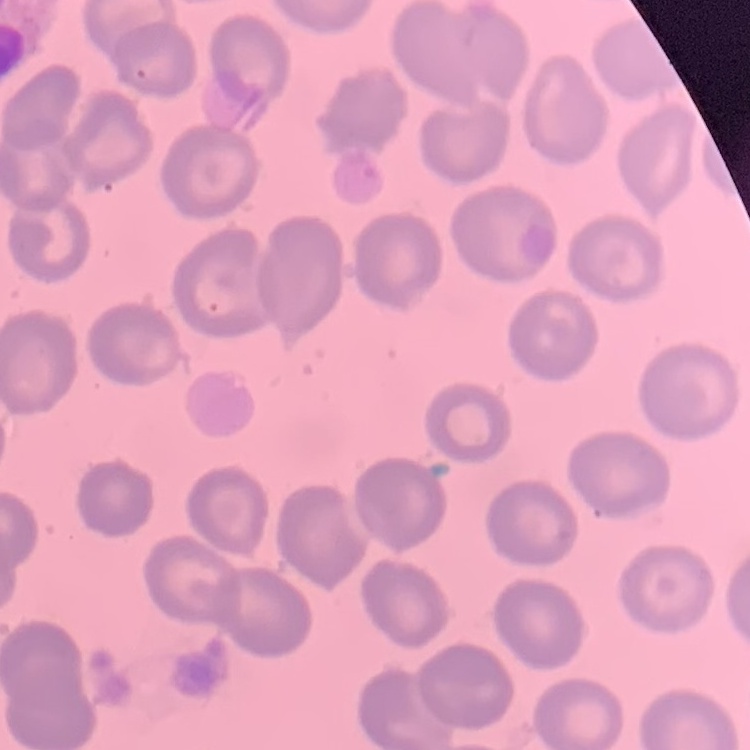
The erythrocytes exhibit no rouleaux formation. Field's or Giemsa stain. Thin blood smear. One tile cut from a larger photomicrograph.